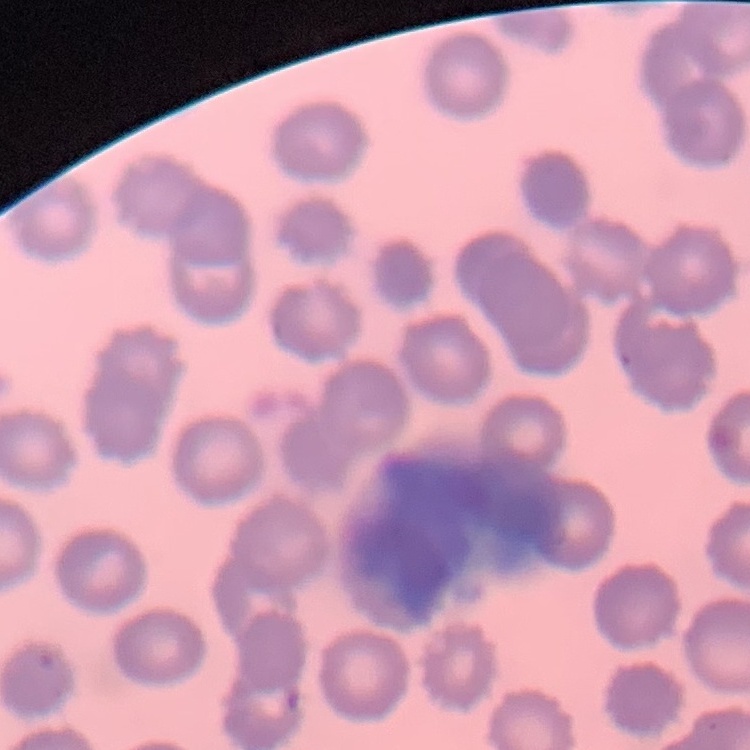

{
  "red_blood_cell_morphology": "no rouleaux formation",
  "stain": "Field's or Giemsa",
  "image_type": "one tile cut from a larger photomicrograph",
  "preparation": "thin blood film"
}